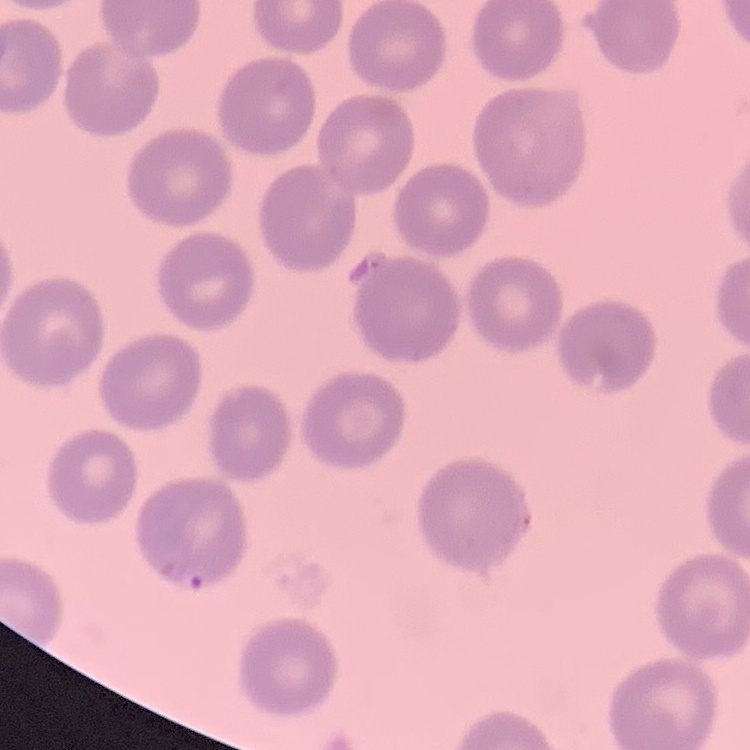

{
  "red_blood_cell_morphology": "no rouleaux formation",
  "image_type": "square crop of a larger photomicrograph",
  "preparation": "thin peripheral smear",
  "stain": "Field's or Giemsa"
}